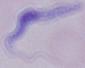 1000x magnification. A trypanosome is seen. Micrograph.